Report the malaria status of this cell.
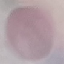
Uninfected.

Automatically extracted cell patch, resized to 64 × 64 pixels. Photographed with a smartphone camera at the microscope eyepiece. Thin blood film. Giemsa-stained preparation.